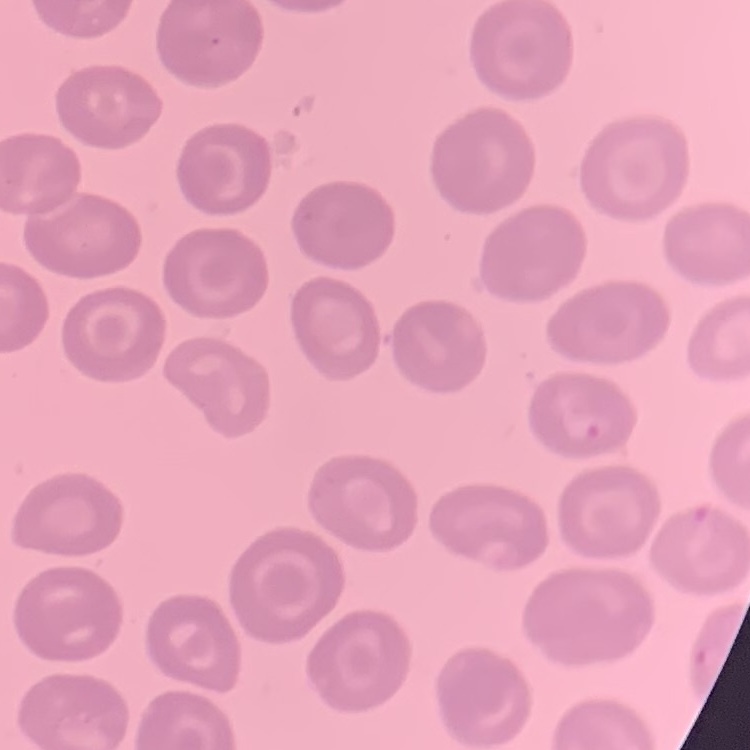 The erythrocytes exhibit no rouleaux formation. Thin peripheral smear. Field's or Giemsa stain. Square crop of a larger photomicrograph.